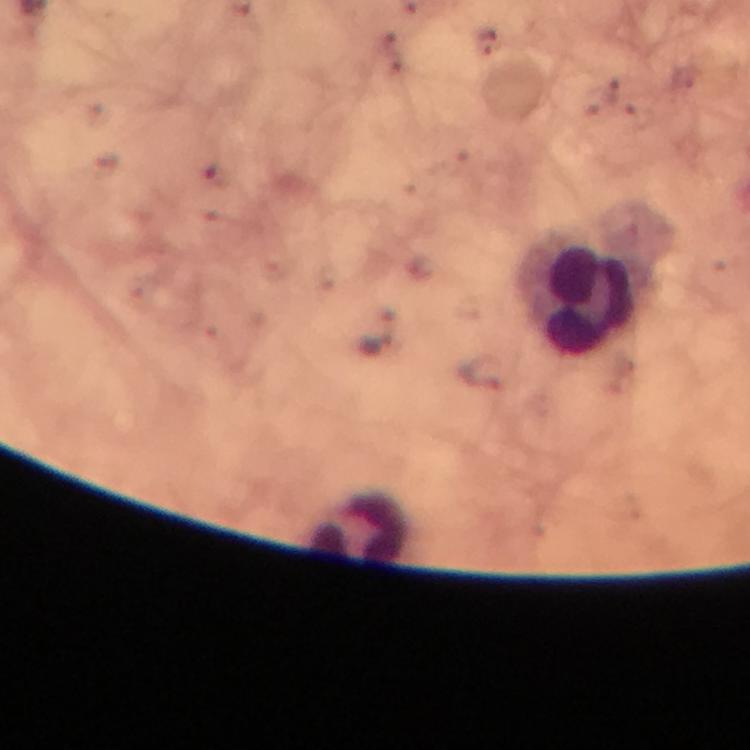 Approximate centers as {x, y} in pixels. Leukocyte locations: {580, 295}, {355, 529}. Giemsa-stained preparation. Thick smear. Immersion oil was used. A crop from one field of view. Plasmodium parasites: none detected. From a diagnostic examination for malaria. Image is 750×750 pixels. Photographed with a smartphone mounted on the microscope. At 100x magnification.